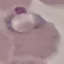

Summary:
  - Malaria status: parasitized
  - Preparation: thin blood film
  - Stain: Giemsa
  - Capture: smartphone camera at the microscope eyepiece
  - Image type: cell patch, automatically extracted from a larger field of view and resized to 64 × 64 pixels